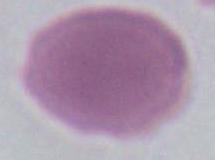

Summary:
  - Magnification: 1000x
  - Identification: red blood cell
  - Modality: photomicrograph